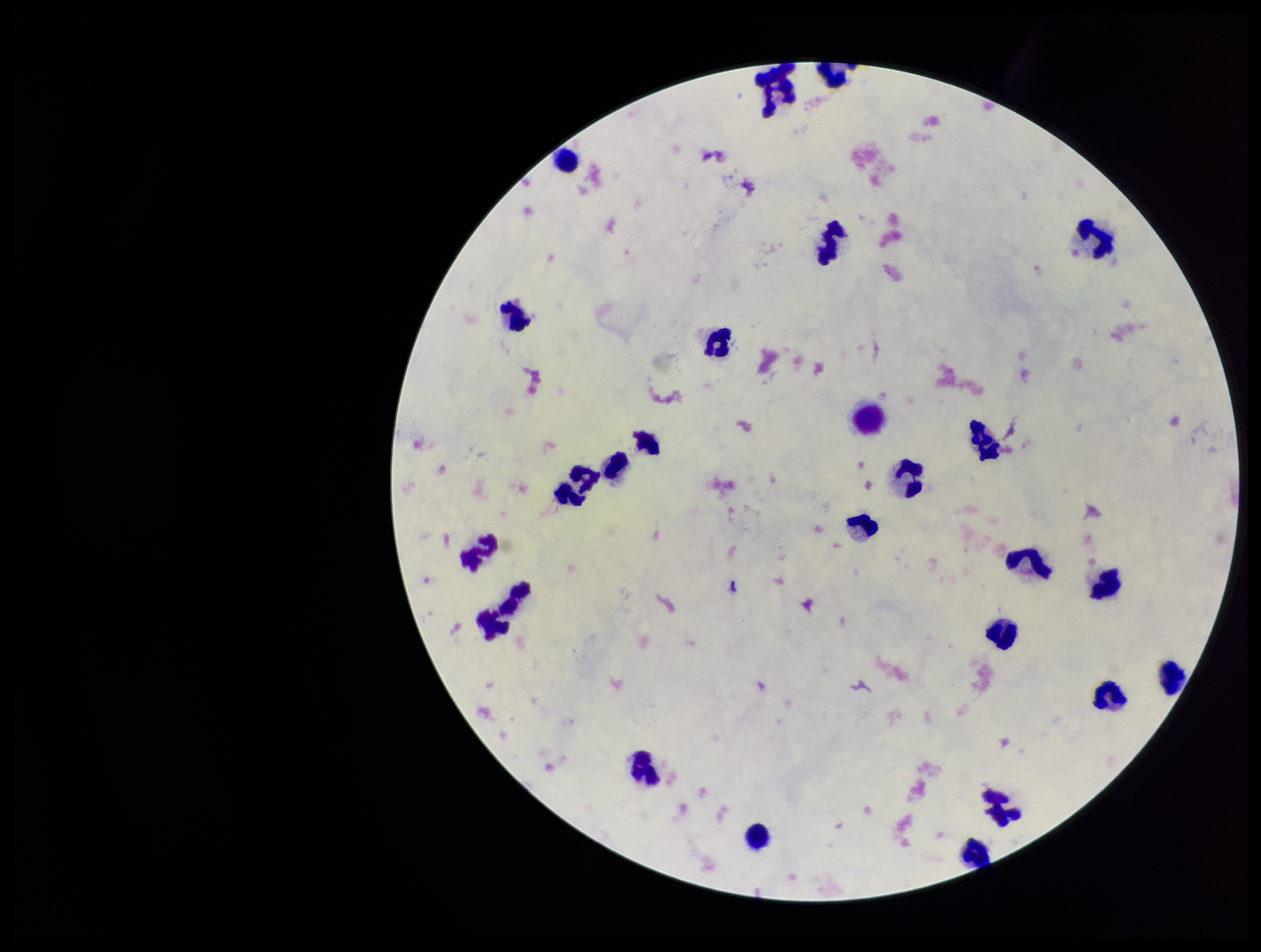

Summary:
  - Capture: smartphone photograph through the microscope eyepiece
  - Plasmodium parasites: none identified
  - Parasite count: 0
  - Patient malaria status: negative
  - Image size: 1261×952 pixels
  - Field of view: one from this slide
  - Stain: Giemsa
  - Leukocyte count: 25
  - Preparation: thick blood smear